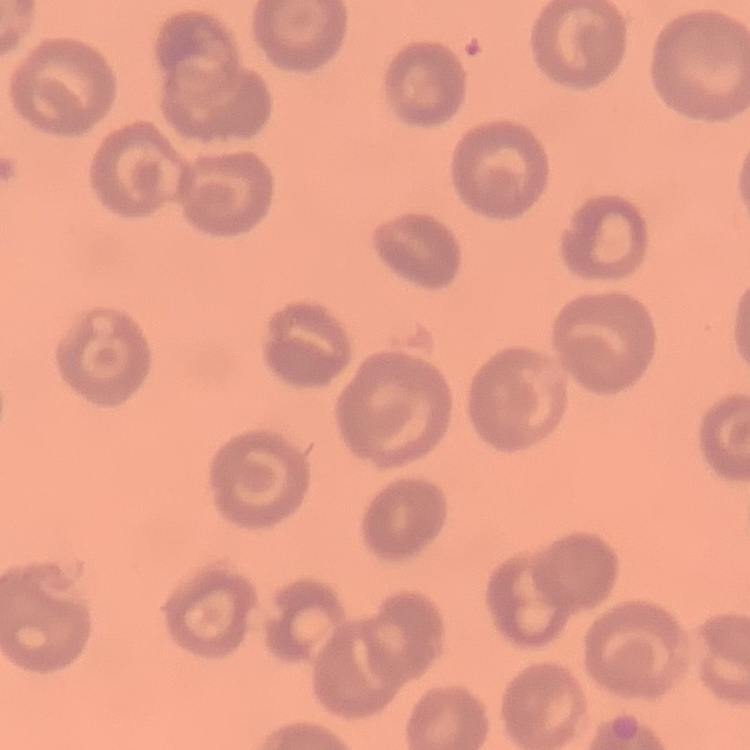
Summary:
  - Erythrocyte morphology: no rouleaux formation
  - Stain: Field's or Giemsa
  - Image type: one tile cut from a larger photomicrograph
  - Preparation: thin blood film